Identify the parasite.
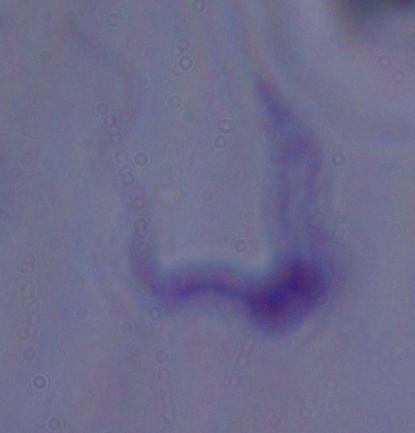
This is a trypanosome.

1000x magnification. Micrograph.